Assess this cell for malaria.
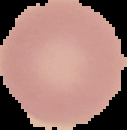

Uninfected.

image type = segmented cell region on a black background
image size = 127×130 pixels
preparation = thin blood smear